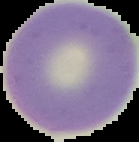
Cell region segmented out of the field of view; the surrounding area is masked to black. Image is 139×142 pixels. From a thin blood smear. Malaria status: uninfected.